Identify the blood parasite species.
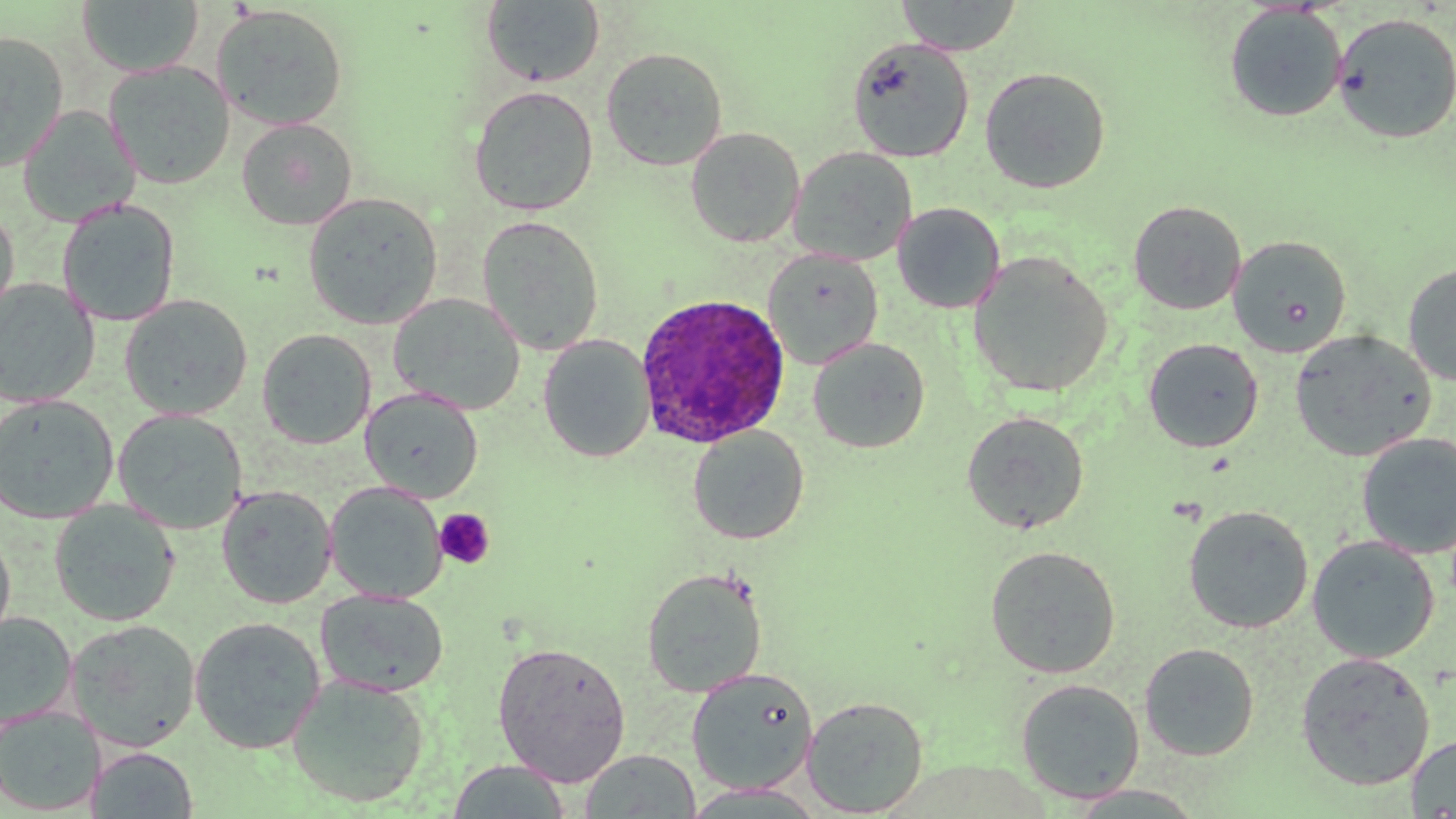

Plasmodium ovale.

platelet locations = approximate bounding boxes as named x1/y1/x2/y2 corners in pixels: (x1=434, y1=508, x2=495, y2=569)
Plasmodium ovale-infected red blood cell locations = approximate bounding boxes as named x1/y1/x2/y2 corners in pixels: (x1=633, y1=292, x2=793, y2=450)
field of view = one of a larger specimen
stain = May-Grünwald-Giemsa
preparation = thin blood film
magnification = 1000x
image size = 1456×819 pixels
uninfected red blood cell locations = approximate bounding boxes as named x1/y1/x2/y2 corners in pixels: (x1=895, y1=0, x2=1023, y2=56), (x1=76, y1=1, x2=205, y2=77), (x1=480, y1=1, x2=605, y2=87), (x1=210, y1=4, x2=349, y2=131), (x1=1224, y1=4, x2=1347, y2=122), (x1=1331, y1=12, x2=1456, y2=144), (x1=0, y1=30, x2=69, y2=171), (x1=847, y1=38, x2=974, y2=162), (x1=601, y1=47, x2=728, y2=171), (x1=6, y1=52, x2=106, y2=206), (x1=103, y1=61, x2=235, y2=190), (x1=979, y1=67, x2=1111, y2=194), (x1=469, y1=85, x2=598, y2=216), (x1=19, y1=106, x2=140, y2=227), (x1=236, y1=117, x2=358, y2=230), (x1=685, y1=126, x2=805, y2=247), (x1=788, y1=147, x2=917, y2=267), (x1=302, y1=191, x2=443, y2=329), (x1=57, y1=199, x2=180, y2=327), (x1=1128, y1=200, x2=1247, y2=315), (x1=0, y1=202, x2=19, y2=321), (x1=893, y1=203, x2=1006, y2=314), (x1=476, y1=214, x2=605, y2=356), (x1=1227, y1=235, x2=1352, y2=357), (x1=763, y1=248, x2=884, y2=370), (x1=968, y1=251, x2=1114, y2=398), (x1=1403, y1=262, x2=1456, y2=386), (x1=0, y1=278, x2=100, y2=407), (x1=388, y1=293, x2=526, y2=415), (x1=119, y1=294, x2=253, y2=420), (x1=256, y1=328, x2=376, y2=449), (x1=1289, y1=329, x2=1437, y2=462), (x1=538, y1=335, x2=655, y2=463), (x1=808, y1=337, x2=930, y2=453), (x1=1142, y1=337, x2=1264, y2=453), (x1=360, y1=388, x2=483, y2=503), (x1=0, y1=394, x2=118, y2=523), (x1=112, y1=408, x2=248, y2=535), (x1=961, y1=410, x2=1090, y2=534), (x1=687, y1=426, x2=809, y2=544), (x1=1356, y1=432, x2=1456, y2=559), (x1=325, y1=482, x2=447, y2=603), (x1=217, y1=485, x2=337, y2=609), (x1=49, y1=500, x2=180, y2=626), (x1=1183, y1=504, x2=1314, y2=633), (x1=0, y1=527, x2=16, y2=651), (x1=1307, y1=535, x2=1440, y2=663), (x1=984, y1=545, x2=1122, y2=679), (x1=641, y1=567, x2=768, y2=697), (x1=315, y1=588, x2=449, y2=698), (x1=0, y1=613, x2=77, y2=731), (x1=189, y1=616, x2=326, y2=754), (x1=66, y1=619, x2=202, y2=752), (x1=492, y1=641, x2=632, y2=786), (x1=1139, y1=642, x2=1259, y2=761), (x1=1295, y1=652, x2=1435, y2=791), (x1=686, y1=667, x2=819, y2=795), (x1=286, y1=674, x2=430, y2=807), (x1=1015, y1=678, x2=1145, y2=803), (x1=801, y1=695, x2=929, y2=817), (x1=0, y1=705, x2=104, y2=815), (x1=1406, y1=734, x2=1456, y2=817), (x1=88, y1=746, x2=199, y2=818), (x1=580, y1=749, x2=700, y2=818), (x1=446, y1=759, x2=573, y2=818), (x1=677, y1=783, x2=832, y2=818), (x1=1064, y1=785, x2=1209, y2=816)
modality = light microscopy